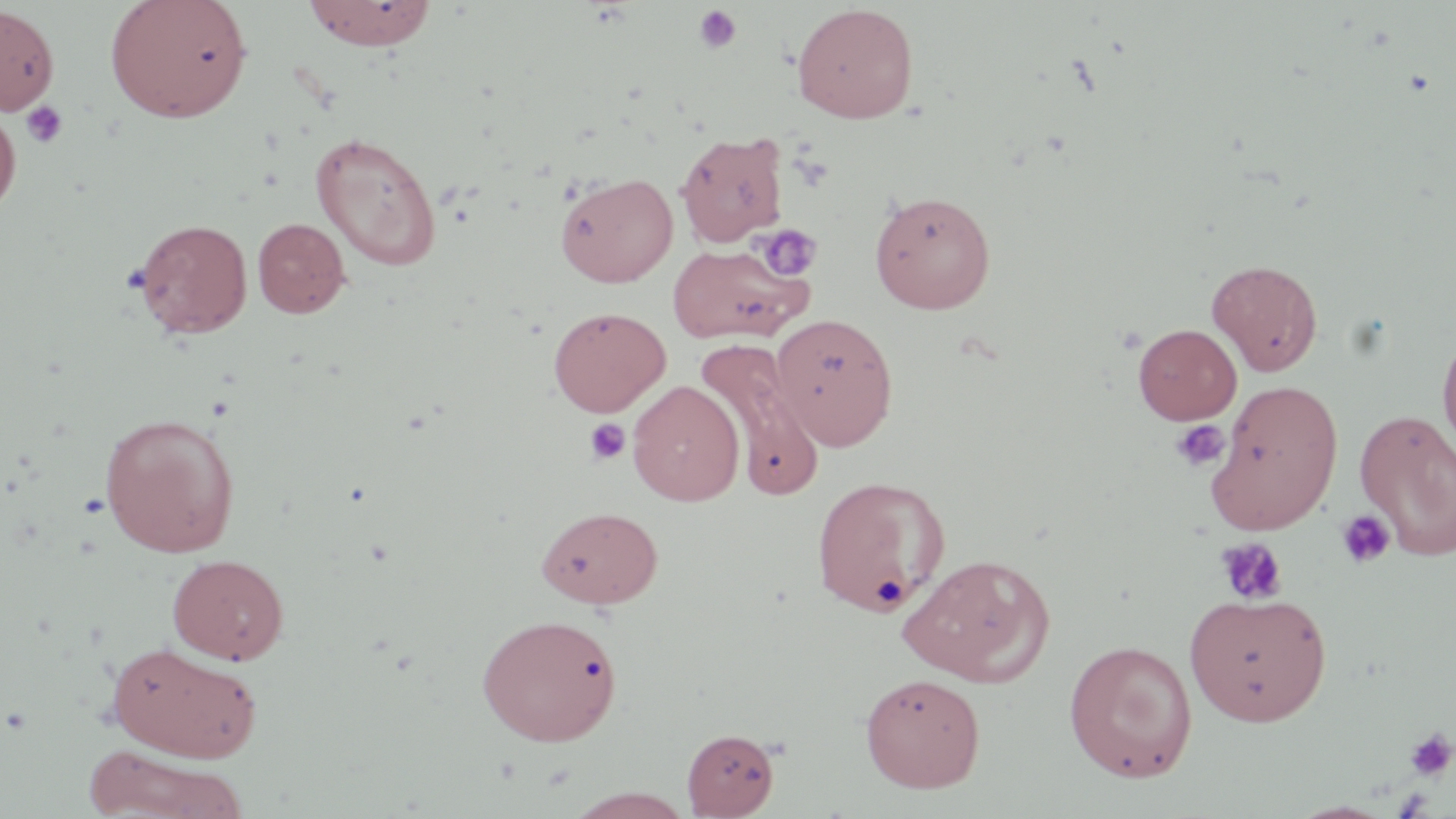
Approximate bounding boxes as named x1/y1/x2/y2 corners in pixels. Uninfected red blood cell locations: (x1=105, y1=0, x2=253, y2=123), (x1=302, y1=1, x2=437, y2=50), (x1=791, y1=3, x2=919, y2=124), (x1=0, y1=5, x2=59, y2=115), (x1=0, y1=107, x2=21, y2=215), (x1=675, y1=131, x2=789, y2=247), (x1=310, y1=132, x2=443, y2=271), (x1=555, y1=172, x2=678, y2=287), (x1=869, y1=189, x2=996, y2=313), (x1=251, y1=217, x2=351, y2=319), (x1=132, y1=218, x2=253, y2=339), (x1=667, y1=242, x2=813, y2=345), (x1=1207, y1=258, x2=1324, y2=376), (x1=547, y1=305, x2=670, y2=417), (x1=771, y1=312, x2=899, y2=450), (x1=1133, y1=323, x2=1241, y2=425), (x1=1436, y1=326, x2=1456, y2=463), (x1=695, y1=339, x2=827, y2=500), (x1=628, y1=380, x2=745, y2=506), (x1=1209, y1=381, x2=1343, y2=533), (x1=1354, y1=407, x2=1456, y2=563), (x1=99, y1=412, x2=241, y2=557), (x1=810, y1=474, x2=951, y2=617), (x1=535, y1=505, x2=663, y2=609), (x1=898, y1=552, x2=1055, y2=687), (x1=168, y1=553, x2=289, y2=665), (x1=1184, y1=591, x2=1332, y2=727), (x1=477, y1=612, x2=622, y2=746), (x1=1062, y1=639, x2=1199, y2=782), (x1=106, y1=641, x2=262, y2=763), (x1=859, y1=672, x2=986, y2=793), (x1=681, y1=728, x2=779, y2=817), (x1=81, y1=745, x2=248, y2=819), (x1=564, y1=788, x2=697, y2=818). Platelet locations: (x1=693, y1=5, x2=743, y2=54), (x1=20, y1=101, x2=68, y2=150), (x1=753, y1=224, x2=823, y2=282), (x1=583, y1=418, x2=630, y2=465), (x1=1171, y1=419, x2=1230, y2=473), (x1=1336, y1=509, x2=1395, y2=569), (x1=1214, y1=537, x2=1288, y2=606), (x1=1404, y1=727, x2=1455, y2=783). Slide-level diagnosis: negative for blood parasites. One field of a larger specimen. 1000x magnification. Image is 1456×819 pixels. Thin blood smear. Optical microscopy. May-Grünwald-Giemsa stain.